Give the extent of all Plasmodium falciparum-infected red blood cells.
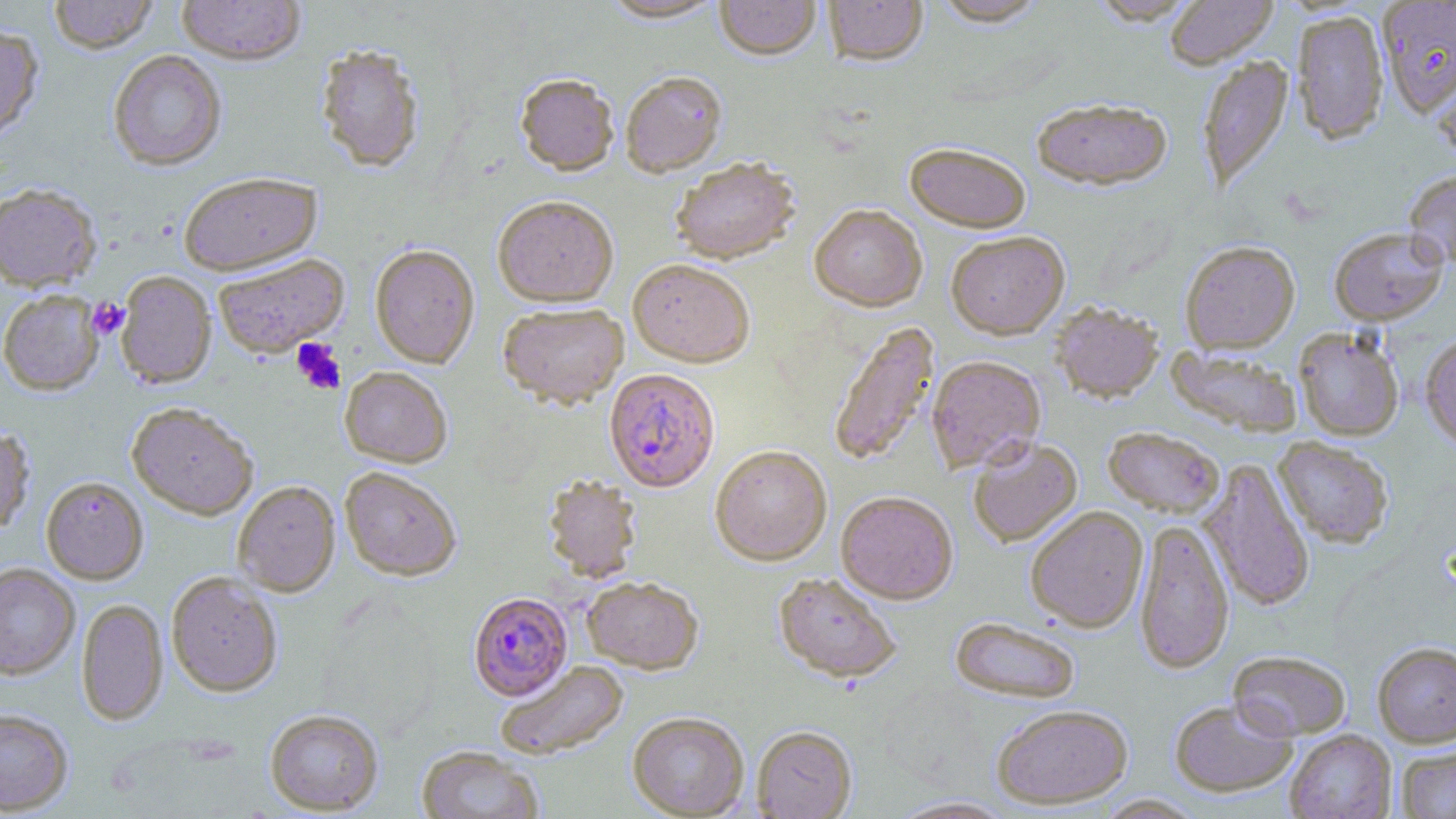
Approximate bounding boxes as (x1, y1, x2, y2) in pixels.
Plasmodium falciparum-infected red blood cells: (604, 370, 721, 493), (468, 592, 573, 701).

slide-level diagnosis = Plasmodium falciparum
field of view = single
image size = 1456×819 pixels
magnification = 1000x
uninfected red blood cell locations = approximate bounding boxes as (x1, y1, x2, y2) in pixels: (48, 0, 159, 53), (177, 0, 305, 66), (599, 0, 725, 24), (715, 0, 821, 62), (823, 0, 927, 68), (930, 0, 1048, 27), (1087, 0, 1203, 26), (1165, 0, 1278, 69), (1378, 1, 1456, 117), (1292, 10, 1389, 145), (0, 22, 44, 143), (315, 43, 425, 173), (109, 50, 227, 171), (1196, 55, 1294, 193), (1432, 70, 1456, 166), (621, 73, 727, 179), (514, 75, 620, 179), (1032, 100, 1173, 192), (904, 145, 1031, 235), (670, 160, 800, 267), (1403, 170, 1456, 270), (179, 173, 322, 275), (0, 183, 102, 292), (493, 198, 619, 308), (809, 206, 927, 313), (1329, 227, 1448, 326), (946, 233, 1070, 341), (1180, 241, 1300, 355), (370, 245, 479, 369), (213, 254, 350, 359), (628, 260, 755, 369), (116, 271, 216, 389), (0, 289, 103, 396), (1050, 303, 1165, 405), (498, 305, 628, 411), (827, 321, 940, 468), (1294, 328, 1404, 441), (1420, 335, 1456, 452), (1166, 345, 1302, 438), (926, 356, 1046, 474), (339, 367, 452, 468), (126, 402, 259, 520), (0, 424, 36, 535), (1103, 428, 1224, 518), (968, 437, 1083, 548), (1273, 437, 1394, 549), (710, 447, 832, 566), (1198, 458, 1315, 613), (340, 467, 462, 581), (542, 475, 643, 584), (41, 476, 148, 584), (232, 481, 341, 597), (835, 492, 958, 606), (1025, 507, 1148, 634), (1133, 518, 1235, 675), (0, 562, 80, 679), (166, 572, 283, 697), (773, 573, 901, 686), (582, 577, 703, 674), (76, 598, 168, 726), (950, 618, 1080, 705), (1372, 641, 1456, 747), (1228, 650, 1352, 741), (495, 660, 630, 760), (1169, 699, 1297, 799), (992, 706, 1133, 810), (0, 708, 73, 815), (264, 708, 384, 816), (627, 713, 749, 818), (751, 727, 857, 819), (1284, 730, 1396, 819), (416, 746, 544, 819), (1396, 746, 1456, 818), (1094, 794, 1206, 818), (887, 796, 1019, 818)
stain = May-Grünwald-Giemsa
modality = optical microscopy
platelet locations = approximate bounding boxes as (x1, y1, x2, y2) in pixels: (88, 298, 129, 340), (291, 338, 346, 395)
preparation = thin blood smear